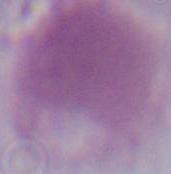

identification = erythrocyte
magnification = 1000x
modality = micrograph